Assess the morphology of the erythrocytes.
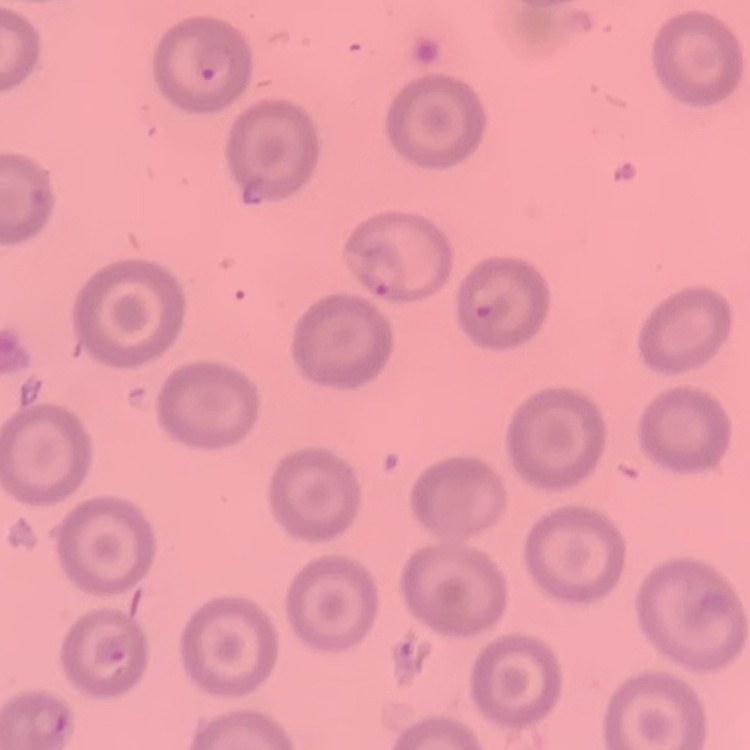

No rouleaux formation.

{
  "preparation": "thin blood film",
  "image_type": "one tile cut from a larger photomicrograph",
  "stain": "Field's or Giemsa"
}